Classify this cell by malaria status.
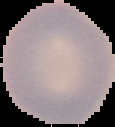

Uninfected.

preparation = thin blood smear
image size = 115×127 pixels
image type = cell region segmented out of the field of view; surrounding area masked to black